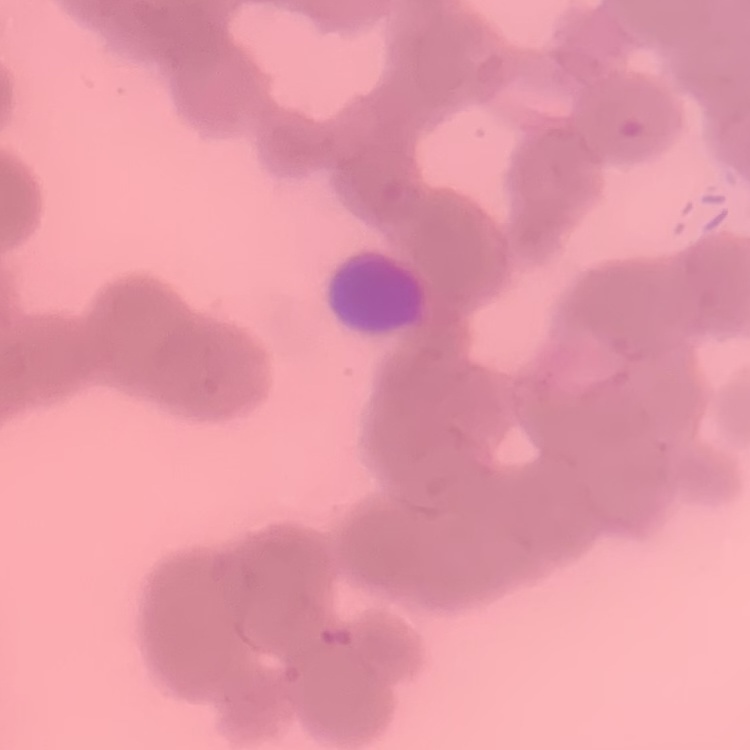

red_blood_cell_morphology: rouleaux formation
preparation: thin blood smear
stain: Field's or Giemsa
image_type: square crop of a larger photomicrograph